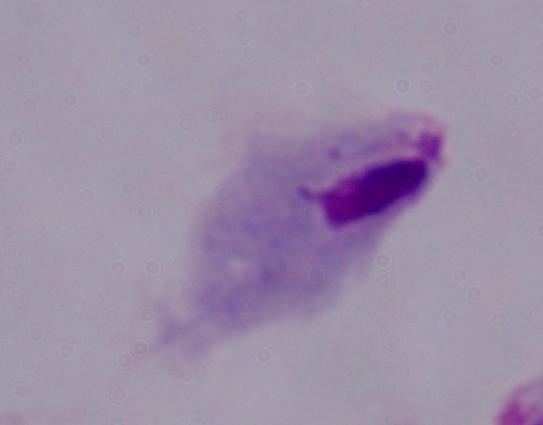 A trichomonad is seen. Micrograph. Captured at 1000x magnification.